Report the malaria status of this cell.
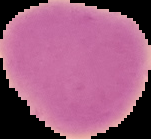
It is uninfected.

The area outside the segmented cell region is set to black. Image is 151×139 pixels. From a thin blood smear.